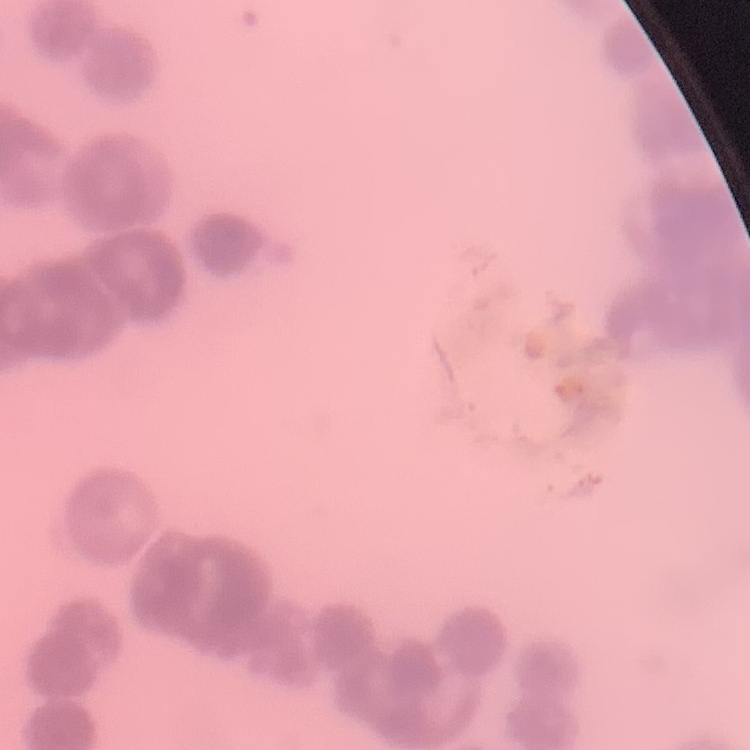

erythrocyte morphology = rouleaux formation
stain = Field's or Giemsa
preparation = thin blood film
image type = one tile cut from a larger photomicrograph